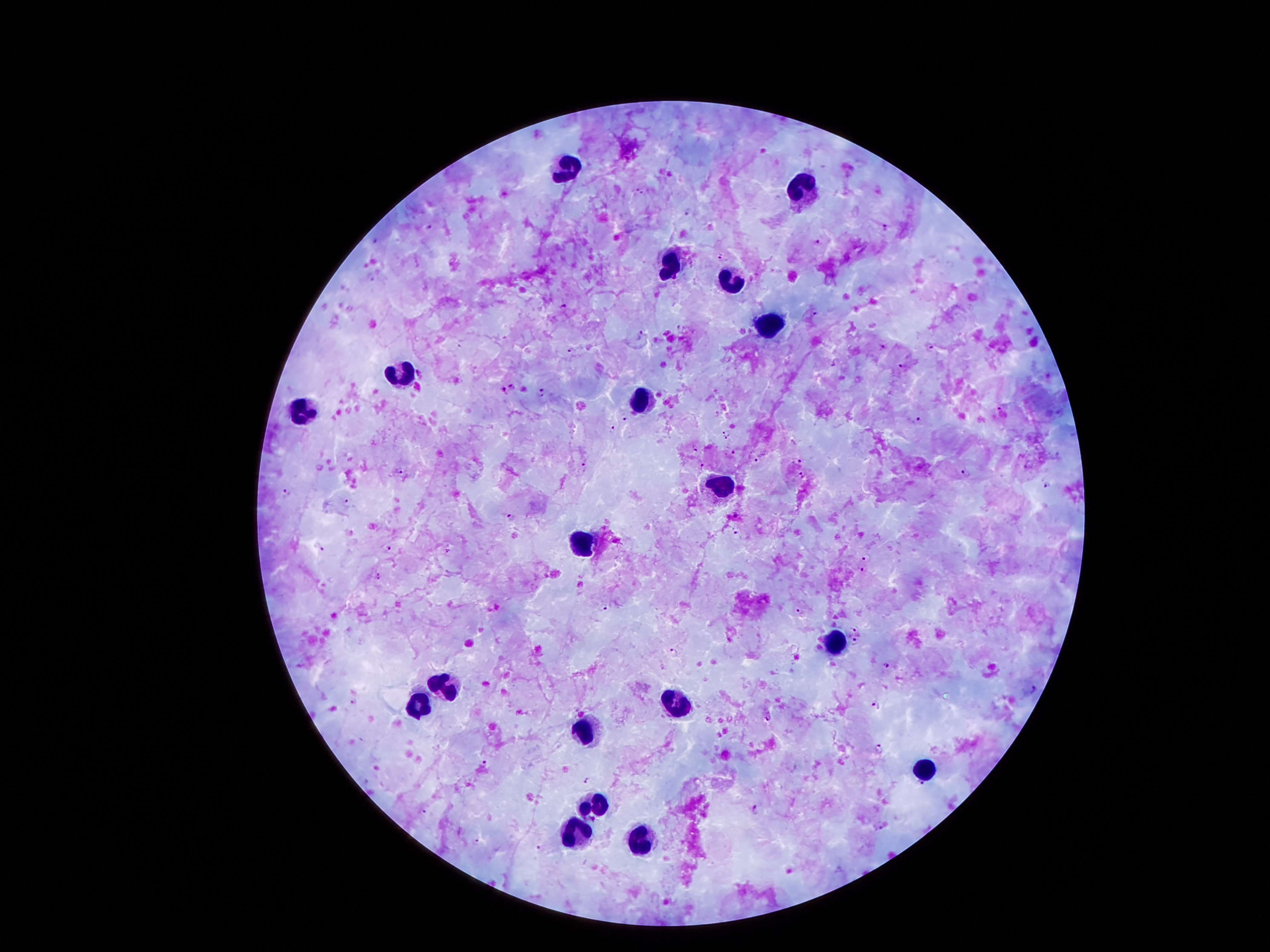 Approximate object centers, in pixels from the top-left corner. Leukocyte locations: (x=567, y=167), (x=803, y=193), (x=671, y=262), (x=732, y=279), (x=767, y=327), (x=404, y=374), (x=643, y=399), (x=305, y=411), (x=719, y=485), (x=580, y=544), (x=839, y=643), (x=447, y=690), (x=678, y=704), (x=417, y=709), (x=585, y=730), (x=923, y=768), (x=595, y=804), (x=577, y=839), (x=643, y=839). Malaria parasite locations: (x=641, y=191), (x=689, y=212), (x=884, y=226), (x=429, y=227), (x=815, y=242), (x=720, y=255), (x=564, y=306), (x=815, y=314), (x=679, y=327), (x=642, y=336), (x=883, y=348), (x=930, y=349), (x=572, y=350), (x=901, y=365), (x=512, y=386), (x=504, y=390), (x=542, y=392), (x=626, y=417), (x=918, y=421), (x=612, y=428), (x=726, y=428), (x=727, y=440), (x=695, y=448), (x=735, y=452), (x=755, y=460), (x=797, y=462), (x=583, y=465), (x=703, y=466), (x=401, y=471), (x=964, y=472), (x=803, y=475), (x=1048, y=485), (x=286, y=492), (x=347, y=501), (x=736, y=515), (x=510, y=516), (x=735, y=530), (x=319, y=548), (x=389, y=549), (x=447, y=551), (x=865, y=558), (x=863, y=569), (x=378, y=576), (x=602, y=606), (x=800, y=611), (x=856, y=630), (x=855, y=642), (x=674, y=653), (x=886, y=664), (x=1033, y=689), (x=355, y=702), (x=876, y=706), (x=767, y=718), (x=879, y=749), (x=483, y=764), (x=588, y=779), (x=922, y=782), (x=757, y=808), (x=425, y=811), (x=881, y=827), (x=475, y=841), (x=538, y=848). Giemsa stain. One field from this slide. 100x magnification. Image is 1270×952 pixels. Photographed through the microscope eyepiece with a smartphone camera. Patient malaria status: infected with Plasmodium falciparum. Thick peripheral-blood smear.